Give the position of every leukocyte visible.
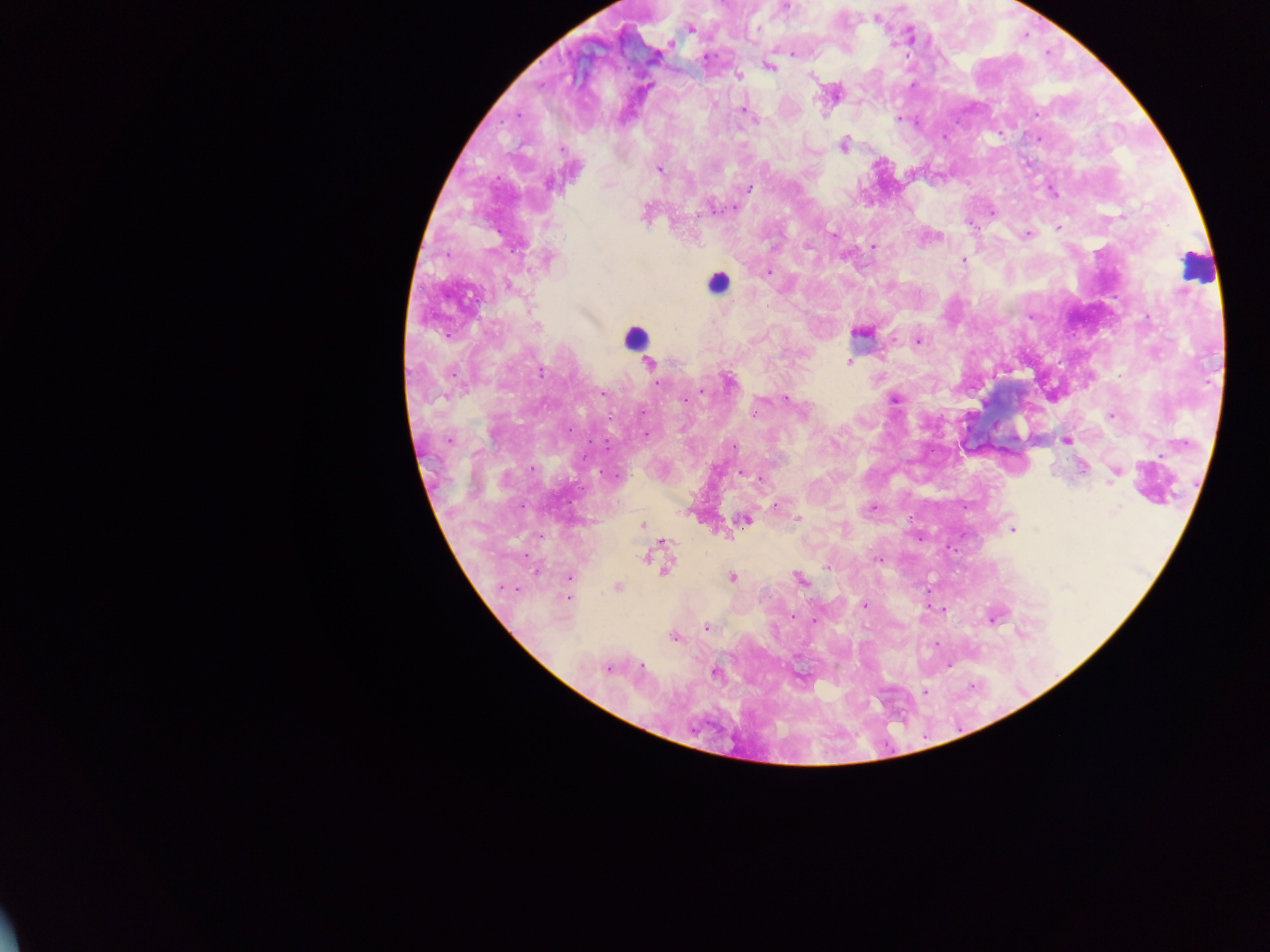
Approximate centers as [x, y] in pixels.
Leukocytes: [1197, 269], [715, 279], [635, 338].

Summary:
  - Malaria parasite locations: [790, 6], [784, 8], [878, 18], [692, 28], [791, 52], [771, 66], [738, 76], [811, 76], [650, 85], [741, 109], [1036, 114], [898, 118], [757, 120], [843, 145], [560, 148], [659, 168], [749, 188], [1053, 191], [710, 206], [733, 207], [647, 214], [1057, 227], [833, 233], [937, 234], [1026, 234], [874, 246], [808, 247], [962, 260], [767, 272], [1147, 316], [918, 340], [848, 362], [542, 373], [653, 378], [727, 379], [658, 383], [702, 392], [786, 397], [896, 399], [684, 401], [756, 407], [643, 433], [448, 440], [1068, 440], [606, 445], [734, 447], [1082, 467], [1117, 472], [742, 474], [873, 506], [1119, 509], [690, 511], [798, 519], [746, 520], [642, 523], [1012, 529], [727, 534], [646, 557], [656, 559], [667, 560], [875, 560], [826, 568], [535, 572], [568, 577], [733, 577], [797, 579], [504, 586], [617, 587], [515, 591], [569, 598], [865, 604], [943, 610], [1001, 613], [791, 615], [993, 618], [815, 621], [705, 628], [1022, 631], [675, 637], [642, 667], [607, 669], [714, 671], [924, 694]
  - Field of view: single
  - Image size: 1270×952 pixels
  - Country: Ghana
  - Preparation: thick blood smear
  - Capture: mobile-phone photograph through a microscope